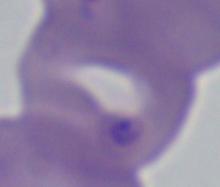

{
  "magnification": "1000x",
  "modality": "photomicrograph",
  "identification": "Babesia"
}